Locate platelets.
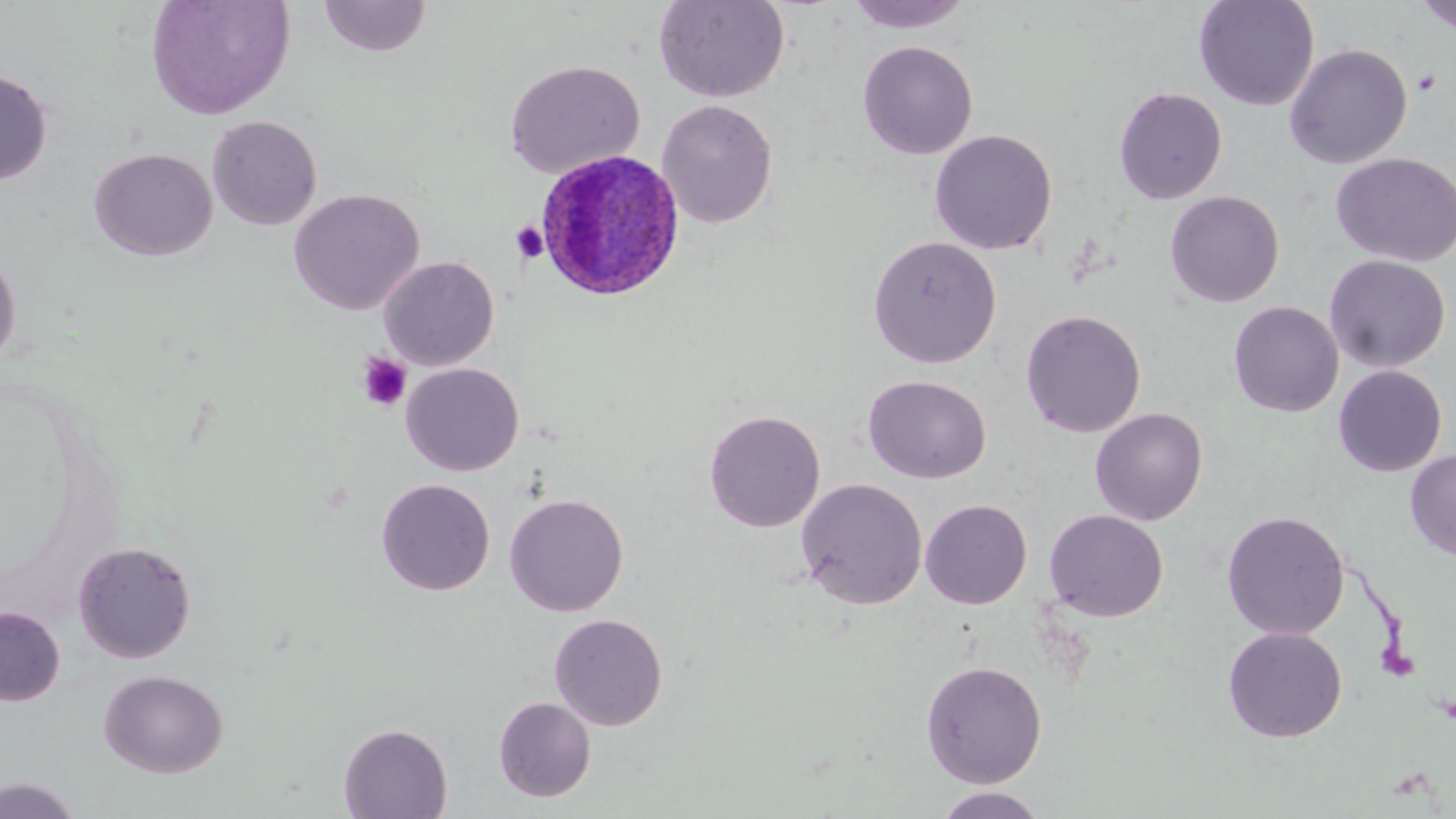

Approximate bounding boxes as named x1/y1/x2/y2 corners in pixels.
Platelets: (x1=1412, y1=69, x2=1442, y2=96), (x1=510, y1=221, x2=549, y2=264), (x1=356, y1=352, x2=412, y2=411).

Summary:
  - Plasmodium ovale-infected red blood cell locations: (x1=535, y1=148, x2=687, y2=301)
  - Uninfected red blood cell locations: (x1=145, y1=0, x2=294, y2=120), (x1=319, y1=0, x2=433, y2=58), (x1=653, y1=0, x2=790, y2=103), (x1=843, y1=0, x2=976, y2=33), (x1=1193, y1=0, x2=1320, y2=111), (x1=1414, y1=1, x2=1456, y2=35), (x1=857, y1=40, x2=978, y2=160), (x1=1284, y1=43, x2=1412, y2=169), (x1=504, y1=59, x2=645, y2=179), (x1=0, y1=69, x2=53, y2=185), (x1=1113, y1=86, x2=1227, y2=204), (x1=656, y1=99, x2=778, y2=229), (x1=207, y1=115, x2=322, y2=230), (x1=929, y1=129, x2=1058, y2=255), (x1=89, y1=147, x2=217, y2=262), (x1=1330, y1=152, x2=1456, y2=267), (x1=289, y1=188, x2=425, y2=315), (x1=1165, y1=190, x2=1284, y2=308), (x1=867, y1=235, x2=1002, y2=369), (x1=0, y1=249, x2=22, y2=370), (x1=1324, y1=254, x2=1451, y2=372), (x1=378, y1=256, x2=499, y2=371), (x1=1228, y1=301, x2=1344, y2=417), (x1=1021, y1=309, x2=1146, y2=438), (x1=400, y1=363, x2=524, y2=476), (x1=1333, y1=365, x2=1447, y2=477), (x1=862, y1=374, x2=992, y2=484), (x1=1090, y1=407, x2=1208, y2=526), (x1=704, y1=409, x2=826, y2=533), (x1=1405, y1=449, x2=1456, y2=560), (x1=376, y1=478, x2=495, y2=596), (x1=796, y1=478, x2=928, y2=609), (x1=504, y1=493, x2=628, y2=617), (x1=920, y1=499, x2=1032, y2=609), (x1=1044, y1=509, x2=1168, y2=621), (x1=1221, y1=510, x2=1350, y2=640), (x1=72, y1=540, x2=197, y2=663), (x1=0, y1=606, x2=65, y2=705), (x1=548, y1=612, x2=668, y2=730), (x1=1222, y1=626, x2=1347, y2=743), (x1=920, y1=660, x2=1047, y2=788), (x1=98, y1=669, x2=228, y2=778), (x1=493, y1=696, x2=596, y2=802), (x1=338, y1=723, x2=452, y2=818), (x1=0, y1=776, x2=83, y2=818), (x1=929, y1=787, x2=1052, y2=818)
  - Slide-level diagnosis: Plasmodium ovale
  - Modality: light microscopy
  - Field of view: one of a larger specimen
  - Magnification: 1000x
  - Preparation: thin blood smear
  - Stain: May-Grünwald-Giemsa
  - Image size: 1456×819 pixels